Name the cell type shown.
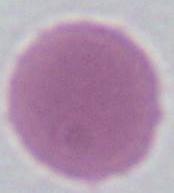
This is an erythrocyte.

Micrograph. 1000x magnification.